Assess the morphology of the red blood cells.
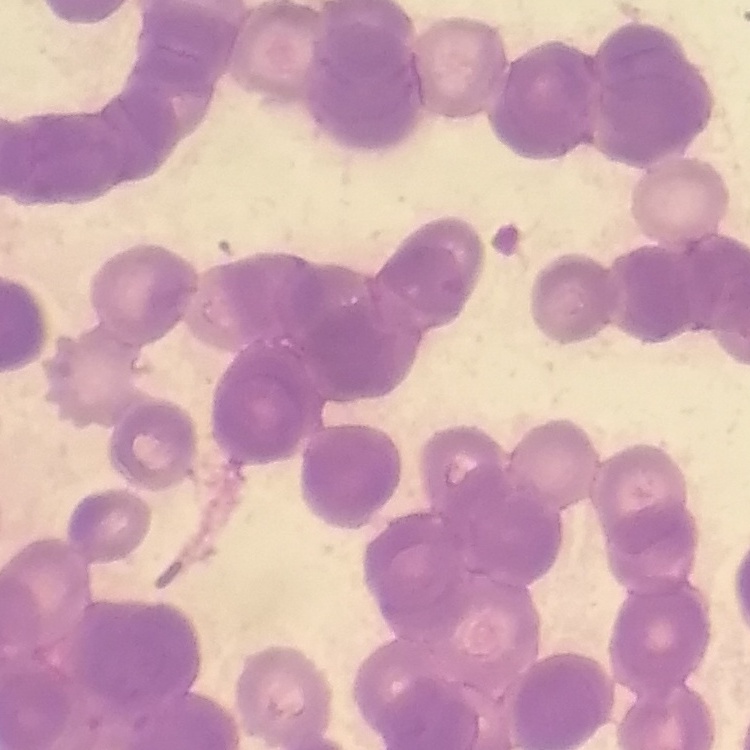
They show rouleaux formation.

Summary:
  - Image type: square crop of a larger photomicrograph
  - Stain: Field's or Giemsa
  - Preparation: thin blood film